Locate every white blood cell.
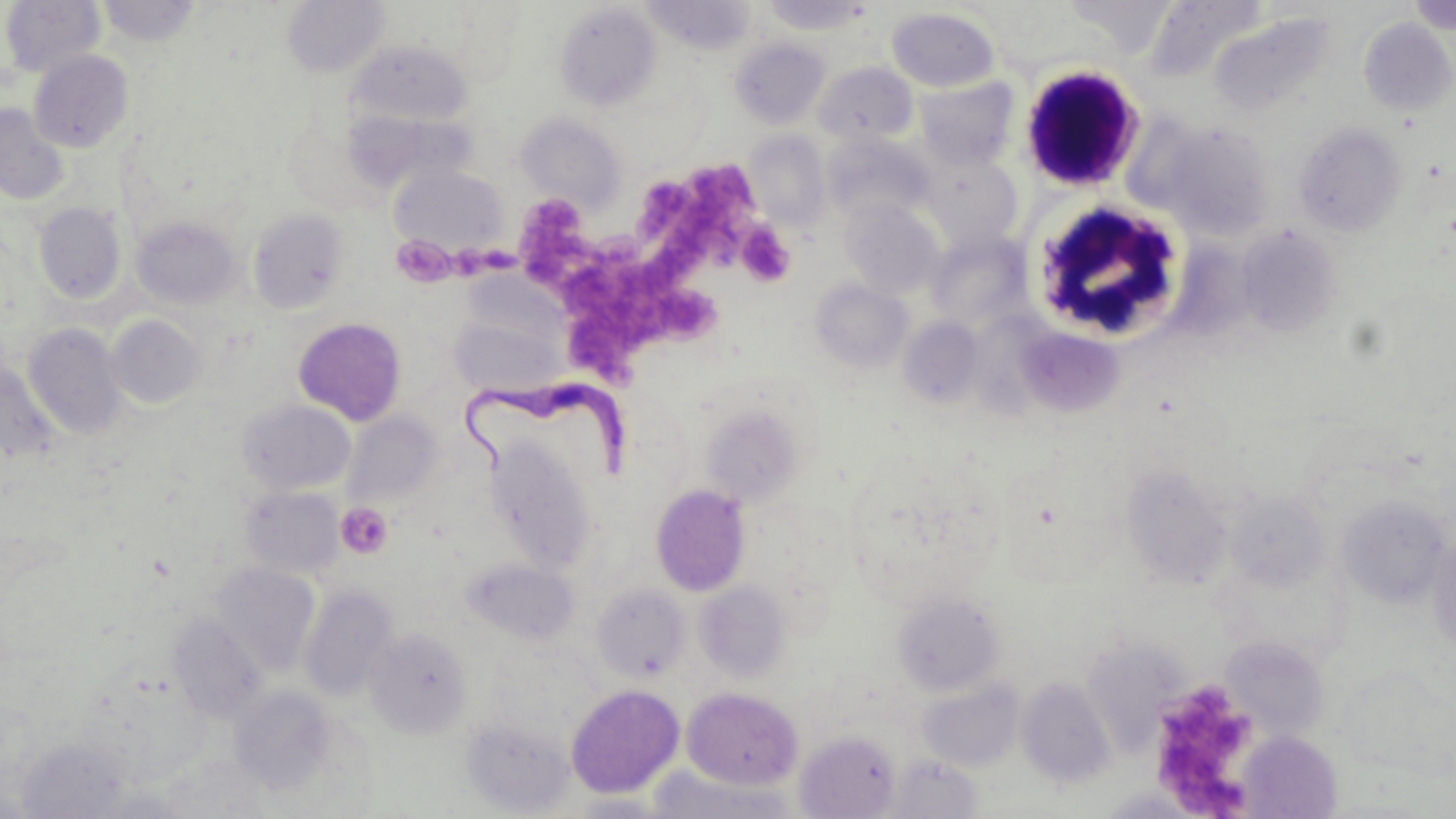
Approximate bounding boxes as named x1/y1/x2/y2 corners in pixels.
White blood cells: (x1=1018, y1=62, x2=1146, y2=191), (x1=1029, y1=199, x2=1190, y2=343).

slide-level diagnosis = Trypanosoma brucei
uninfected red blood cell locations = approximate bounding boxes as named x1/y1/x2/y2 corners in pixels: (x1=761, y1=0, x2=875, y2=35), (x1=1064, y1=0, x2=1178, y2=53), (x1=1408, y1=0, x2=1455, y2=35), (x1=0, y1=1, x2=106, y2=78), (x1=96, y1=1, x2=203, y2=46), (x1=282, y1=1, x2=390, y2=78), (x1=641, y1=1, x2=757, y2=55), (x1=554, y1=3, x2=662, y2=111), (x1=1145, y1=3, x2=1269, y2=82), (x1=886, y1=7, x2=999, y2=92), (x1=1207, y1=12, x2=1335, y2=117), (x1=1359, y1=18, x2=1456, y2=116), (x1=730, y1=38, x2=830, y2=129), (x1=351, y1=40, x2=472, y2=126), (x1=28, y1=49, x2=134, y2=153), (x1=813, y1=61, x2=918, y2=147), (x1=916, y1=78, x2=1018, y2=170), (x1=0, y1=103, x2=70, y2=206), (x1=516, y1=114, x2=626, y2=210), (x1=1160, y1=122, x2=1275, y2=241), (x1=1294, y1=122, x2=1407, y2=236), (x1=744, y1=131, x2=831, y2=231), (x1=824, y1=134, x2=936, y2=222), (x1=923, y1=155, x2=1022, y2=249), (x1=390, y1=165, x2=506, y2=255), (x1=840, y1=197, x2=945, y2=299), (x1=34, y1=202, x2=126, y2=305), (x1=248, y1=209, x2=350, y2=314), (x1=132, y1=217, x2=239, y2=309), (x1=1235, y1=224, x2=1342, y2=339), (x1=925, y1=231, x2=1031, y2=331), (x1=810, y1=279, x2=913, y2=373), (x1=449, y1=308, x2=569, y2=400), (x1=107, y1=315, x2=207, y2=408), (x1=898, y1=317, x2=984, y2=409), (x1=294, y1=318, x2=407, y2=425), (x1=23, y1=323, x2=127, y2=439), (x1=1013, y1=325, x2=1125, y2=420), (x1=0, y1=360, x2=58, y2=465), (x1=239, y1=400, x2=355, y2=495), (x1=701, y1=404, x2=805, y2=506), (x1=343, y1=412, x2=442, y2=508), (x1=487, y1=439, x2=595, y2=572), (x1=1122, y1=463, x2=1234, y2=589), (x1=650, y1=484, x2=751, y2=596), (x1=241, y1=485, x2=345, y2=579), (x1=1225, y1=492, x2=1329, y2=591), (x1=1337, y1=497, x2=1451, y2=609), (x1=1428, y1=533, x2=1456, y2=657), (x1=465, y1=557, x2=578, y2=645), (x1=211, y1=562, x2=320, y2=676), (x1=694, y1=581, x2=791, y2=682), (x1=299, y1=585, x2=398, y2=703), (x1=592, y1=585, x2=691, y2=682), (x1=892, y1=593, x2=1005, y2=696), (x1=168, y1=612, x2=267, y2=723), (x1=364, y1=627, x2=473, y2=740), (x1=1221, y1=635, x2=1329, y2=740), (x1=1080, y1=637, x2=1192, y2=757), (x1=1337, y1=665, x2=1455, y2=777), (x1=916, y1=678, x2=1025, y2=772), (x1=1017, y1=678, x2=1115, y2=789), (x1=565, y1=683, x2=685, y2=799), (x1=228, y1=686, x2=337, y2=794), (x1=682, y1=687, x2=802, y2=789), (x1=460, y1=717, x2=575, y2=816), (x1=795, y1=730, x2=901, y2=818), (x1=1236, y1=731, x2=1343, y2=818), (x1=887, y1=755, x2=984, y2=818), (x1=644, y1=767, x2=797, y2=818), (x1=1095, y1=787, x2=1212, y2=819)
image size = 1456×819 pixels
magnification = 1000x
field of view = single
modality = optical microscopy
preparation = thin blood film
Trypanosoma brucei locations = approximate bounding boxes as named x1/y1/x2/y2 corners in pixels: (x1=457, y1=375, x2=637, y2=483)
stain = May-Grünwald-Giemsa
platelet locations = approximate bounding boxes as named x1/y1/x2/y2 corners in pixels: (x1=686, y1=164, x2=760, y2=227), (x1=642, y1=181, x2=692, y2=243), (x1=508, y1=195, x2=595, y2=286), (x1=666, y1=208, x2=737, y2=277), (x1=736, y1=223, x2=796, y2=287), (x1=393, y1=240, x2=458, y2=283), (x1=450, y1=243, x2=517, y2=277), (x1=566, y1=258, x2=720, y2=380), (x1=336, y1=501, x2=393, y2=559), (x1=1147, y1=679, x2=1264, y2=812)